Describe the morphology of the red blood cells.
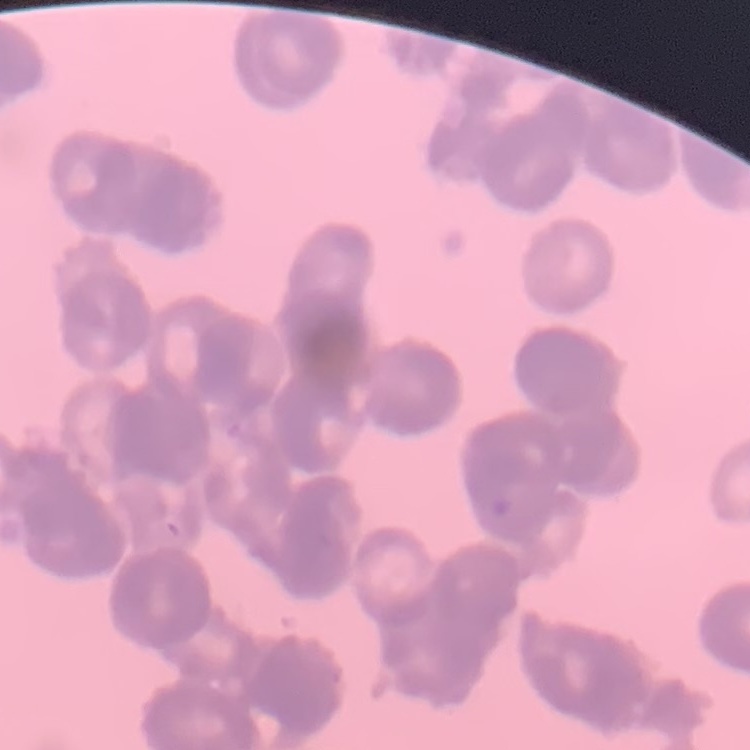
They show rouleaux formation.

Thin blood film. Field's or Giemsa stain. Square crop of a larger photomicrograph.